State the blood parasite species.
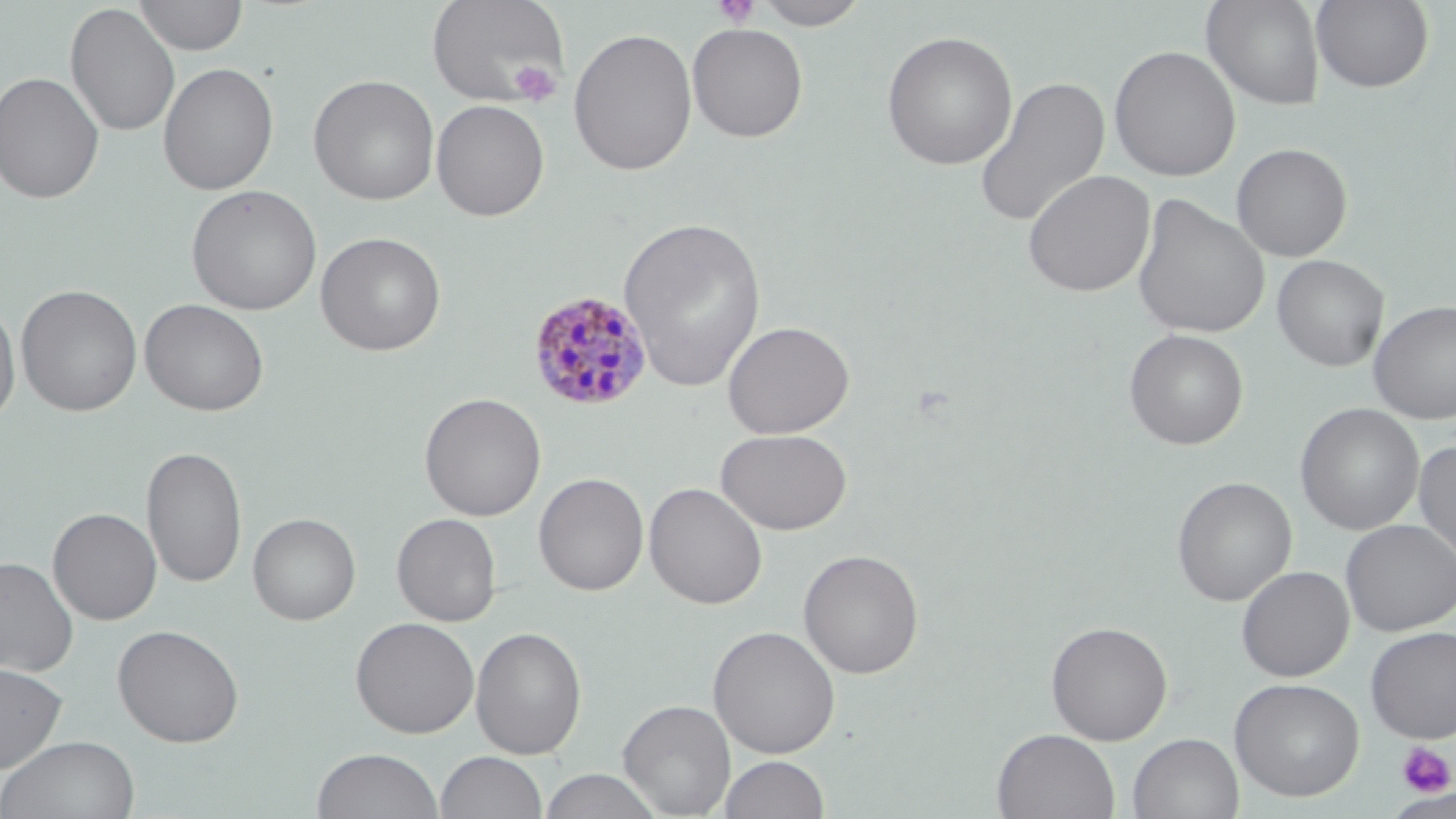

Plasmodium malariae.

platelet locations = approximate bounding boxes as (x1,y1)-(x2,y2) corner pairs in pixels: (712,0)-(762,28), (508,59)-(562,107), (1395,742)-(1454,798)
Plasmodium malariae-infected red blood cell locations = approximate bounding boxes as (x1,y1)-(x2,y2) corner pairs in pixels: (527,291)-(654,411)
image size = 1456×819 pixels
magnification = 1000x
modality = optical microscopy
field of view = one of a larger specimen
uninfected red blood cell locations = approximate bounding boxes as (x1,y1)-(x2,y2) corner pairs in pixels: (133,0)-(248,56), (752,0)-(871,30), (1201,0)-(1325,110), (425,1)-(570,107), (1311,1)-(1434,93), (65,3)-(181,138), (687,23)-(808,142), (568,27)-(697,176), (881,30)-(1018,170), (1109,45)-(1240,182), (157,62)-(279,196), (0,71)-(105,204), (307,74)-(440,205), (973,76)-(1110,230), (431,99)-(549,221), (1231,143)-(1352,262), (1022,169)-(1156,298), (185,184)-(322,315), (1132,194)-(1269,341), (619,216)-(767,393), (315,231)-(446,356), (1272,254)-(1389,372), (15,284)-(142,417), (0,298)-(21,428), (139,298)-(269,416), (1368,299)-(1456,424), (722,320)-(854,439), (1124,329)-(1248,450), (419,392)-(545,521), (1295,403)-(1425,535), (715,428)-(852,534), (1413,440)-(1456,571), (141,445)-(247,588), (534,472)-(648,596), (1171,476)-(1296,605), (644,482)-(767,610), (48,507)-(161,625), (248,512)-(361,625), (391,513)-(501,626), (1340,519)-(1456,636), (797,548)-(925,679), (0,557)-(79,677), (1236,565)-(1354,681), (350,616)-(479,738), (1046,621)-(1172,745), (112,624)-(245,747), (708,625)-(840,759), (470,626)-(587,760), (1365,626)-(1456,743), (0,662)-(68,774), (1228,677)-(1365,801), (618,698)-(736,817), (993,728)-(1119,819), (1128,733)-(1243,819), (0,735)-(141,818), (311,747)-(444,819), (435,751)-(548,819), (719,755)-(831,818), (538,769)-(664,819), (1385,791)-(1456,818)
preparation = thin blood smear
stain = May-Grünwald-Giemsa